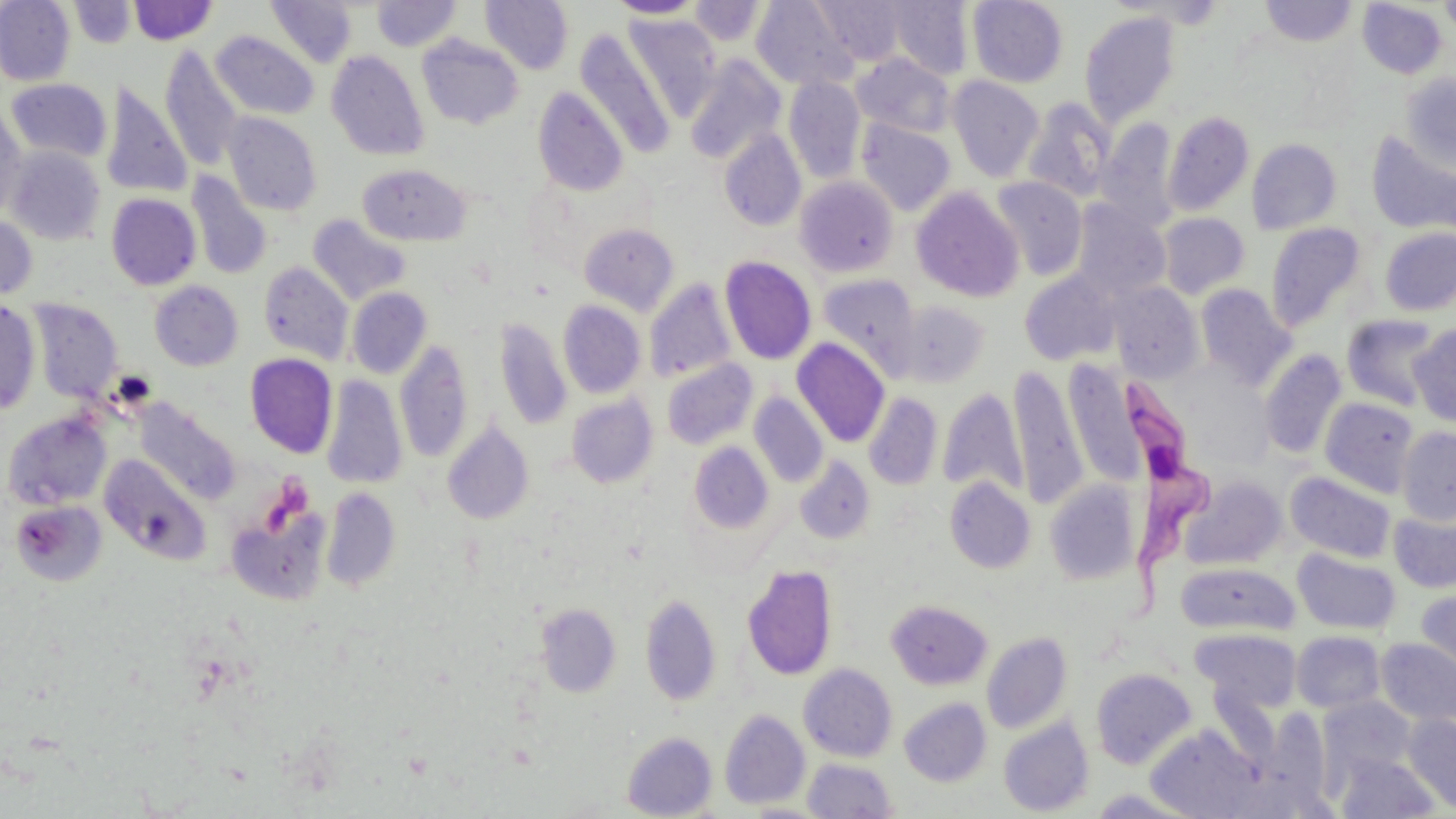
Approximate bounding boxes as [x1, y1, x2, y2] in pixels. Trypanosoma brucei locations: [1123, 389, 1212, 620]. Uninfected red blood cell locations: [0, 0, 75, 86], [480, 0, 574, 74], [608, 0, 707, 19], [815, 0, 908, 66], [968, 0, 1068, 87], [1439, 0, 1456, 43], [69, 1, 136, 48], [128, 1, 217, 45], [266, 1, 358, 68], [372, 1, 460, 51], [690, 1, 764, 44], [751, 1, 858, 90], [888, 1, 974, 79], [1259, 1, 1358, 47], [1357, 1, 1446, 79], [1079, 11, 1182, 129], [623, 15, 722, 122], [210, 30, 319, 119], [575, 31, 676, 158], [417, 35, 524, 130], [159, 46, 243, 171], [326, 50, 430, 161], [852, 53, 955, 137], [685, 56, 785, 164], [1401, 73, 1456, 174], [784, 76, 865, 183], [947, 76, 1045, 182], [6, 78, 111, 163], [101, 82, 193, 198], [533, 86, 629, 197], [1022, 98, 1116, 203], [0, 103, 28, 221], [1163, 110, 1254, 216], [223, 113, 322, 215], [857, 119, 956, 215], [1096, 119, 1178, 231], [718, 129, 806, 231], [1366, 131, 1456, 235], [1247, 138, 1341, 234], [6, 146, 105, 245], [358, 164, 471, 246], [185, 171, 273, 281], [794, 176, 899, 278], [991, 178, 1087, 280], [912, 187, 1024, 302], [106, 193, 201, 290], [1072, 201, 1170, 301], [1159, 213, 1250, 298], [307, 214, 410, 305], [0, 215, 38, 301], [1265, 222, 1367, 331], [579, 223, 679, 315], [1380, 227, 1456, 317], [720, 256, 817, 364], [259, 261, 354, 364], [1019, 270, 1121, 366], [816, 274, 921, 379], [644, 279, 737, 383], [149, 281, 243, 371], [1109, 282, 1203, 383], [1196, 284, 1296, 389], [347, 287, 432, 379], [27, 299, 123, 403], [896, 299, 990, 388], [0, 300, 41, 416], [558, 300, 646, 399], [1341, 314, 1444, 411], [494, 316, 572, 431], [1408, 324, 1456, 427], [792, 337, 891, 448], [395, 339, 474, 463], [1259, 348, 1347, 459], [244, 353, 337, 458], [1066, 357, 1144, 495], [661, 358, 758, 449], [1009, 364, 1088, 507], [321, 375, 407, 490], [937, 386, 1026, 497], [749, 392, 828, 488], [863, 392, 942, 490], [566, 394, 658, 487], [1319, 398, 1419, 498], [134, 401, 237, 502], [3, 411, 111, 510], [442, 420, 534, 525], [1397, 426, 1456, 524], [688, 442, 775, 534], [100, 455, 210, 564], [794, 455, 875, 544], [1286, 471, 1396, 563], [1180, 475, 1286, 570], [945, 477, 1035, 573], [1044, 478, 1141, 584], [321, 487, 401, 592], [10, 500, 107, 586], [225, 500, 333, 606], [1389, 503, 1456, 593], [1293, 547, 1400, 635], [1175, 562, 1297, 634], [742, 564, 838, 680], [1414, 587, 1456, 686], [640, 592, 722, 707], [886, 599, 992, 689], [535, 603, 621, 697], [1192, 628, 1301, 712], [981, 631, 1072, 734], [1291, 631, 1385, 713], [1375, 638, 1456, 726], [799, 663, 897, 761], [1091, 667, 1196, 769], [1319, 695, 1417, 780], [899, 698, 991, 786], [719, 709, 810, 809], [1402, 712, 1456, 813], [998, 717, 1094, 816], [1145, 726, 1263, 817], [622, 731, 718, 819], [1335, 752, 1440, 818], [803, 758, 898, 818]. Slide-level diagnosis: Trypanosoma brucei. May-Grünwald-Giemsa-stained preparation. Optical microscopy. 1000x magnification. One field of a larger specimen. Image is 1456×819 pixels. Thin blood film.